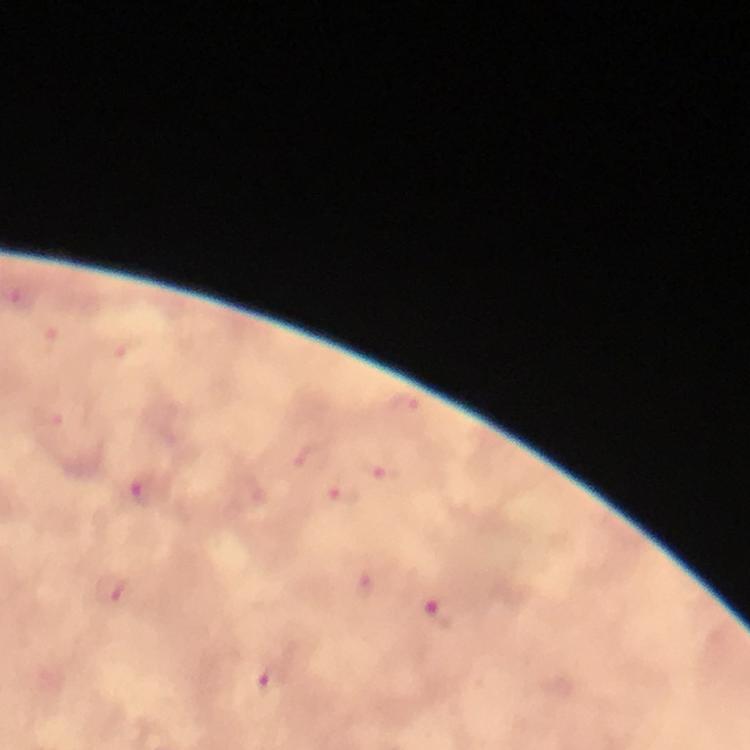

Approximate centers as (x, y) in pixels. Plasmodium parasite locations: (23, 300), (44, 342), (403, 406), (384, 470), (144, 486), (345, 496), (116, 589), (441, 613), (273, 677). Image is 750×750 pixels. From a diagnostic examination for malaria. Photographed through the microscope with a smartphone camera. 100x magnification. Cropped region of a single field of view. Immersion oil was used. Giemsa-stained preparation. Thick blood smear.